Report the malaria status of this cell.
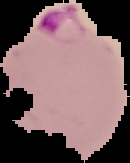

It is parasitized.

image_size: 130×163 pixels
preparation: thin blood smear
image_type: segmented cell region on a black background